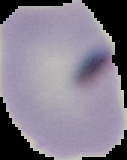
malaria_status: uninfected
image_size: 127×160 pixels
image_type: cell region segmented out of the field of view; surrounding area masked to black
preparation: thin blood film